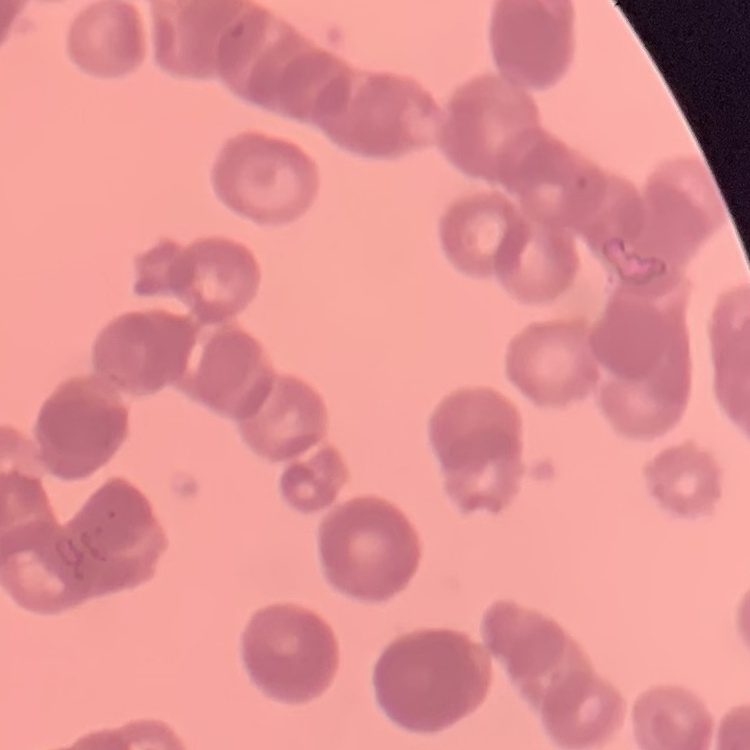
red blood cell morphology = rouleaux formation
stain = Field's or Giemsa
image type = one tile cut from a larger photomicrograph
preparation = thin blood film